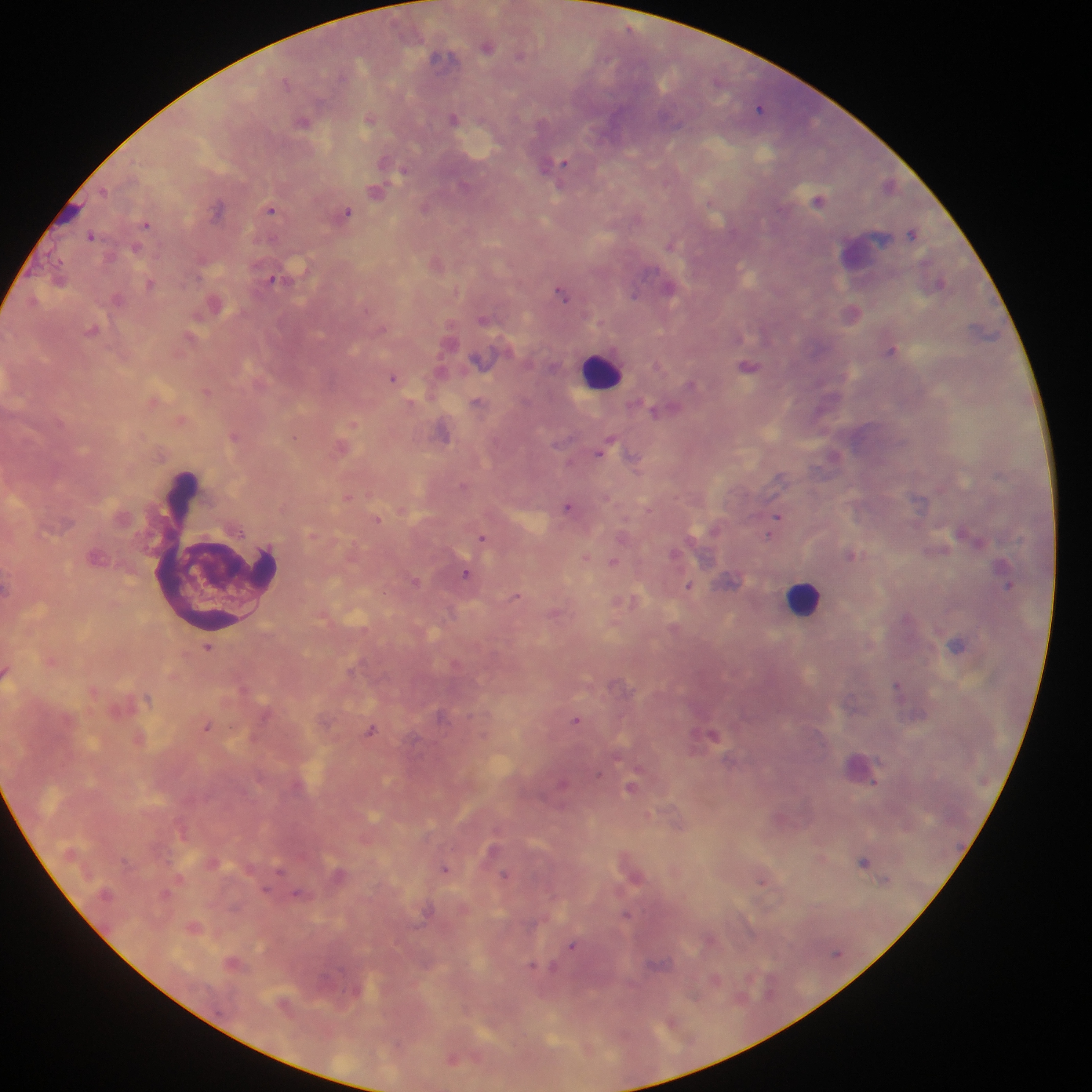

Approximate centers as {x, y} in pixels. Malaria parasite locations: {487, 46}, {442, 56}, {519, 56}, {341, 75}, {286, 82}, {760, 107}, {454, 118}, {369, 119}, {302, 122}, {552, 164}, {562, 164}, {403, 171}, {104, 190}, {376, 190}, {818, 200}, {710, 203}, {425, 208}, {217, 209}, {271, 210}, {346, 211}, {146, 224}, {912, 233}, {91, 235}, {670, 246}, {136, 247}, {274, 280}, {940, 283}, {149, 284}, {670, 289}, {562, 293}, {634, 293}, {118, 299}, {92, 330}, {891, 351}, {749, 366}, {392, 378}, {691, 385}, {206, 392}, {476, 401}, {653, 410}, {353, 424}, {443, 434}, {234, 437}, {295, 438}, {608, 443}, {601, 450}, {634, 459}, {463, 485}, {347, 497}, {567, 507}, {777, 516}, {378, 519}, {962, 532}, {770, 534}, {482, 538}, {673, 554}, {851, 554}, {586, 557}, {613, 562}, {466, 574}, {416, 581}, {1009, 585}, {688, 586}, {516, 597}, {957, 645}, {208, 648}, {896, 686}, {147, 698}, {442, 716}, {576, 720}, {207, 727}, {371, 730}, {713, 734}, {563, 783}, {630, 788}, {864, 861}, {280, 869}, {444, 869}, {505, 874}, {761, 880}, {885, 880}, {266, 890}, {298, 894}, {627, 915}, {572, 946}, {532, 966}, {551, 967}. Leukocyte locations: {601, 370}, {216, 553}, {804, 598}. Mobile-phone photograph taken through the microscope. One field of view. Sample from Ghana. Image is 1092×1092 pixels. Thick blood film.